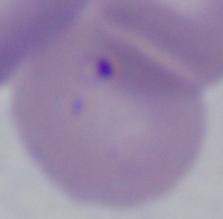

{
  "magnification": "1000x",
  "modality": "micrograph",
  "identification": "Babesia"
}